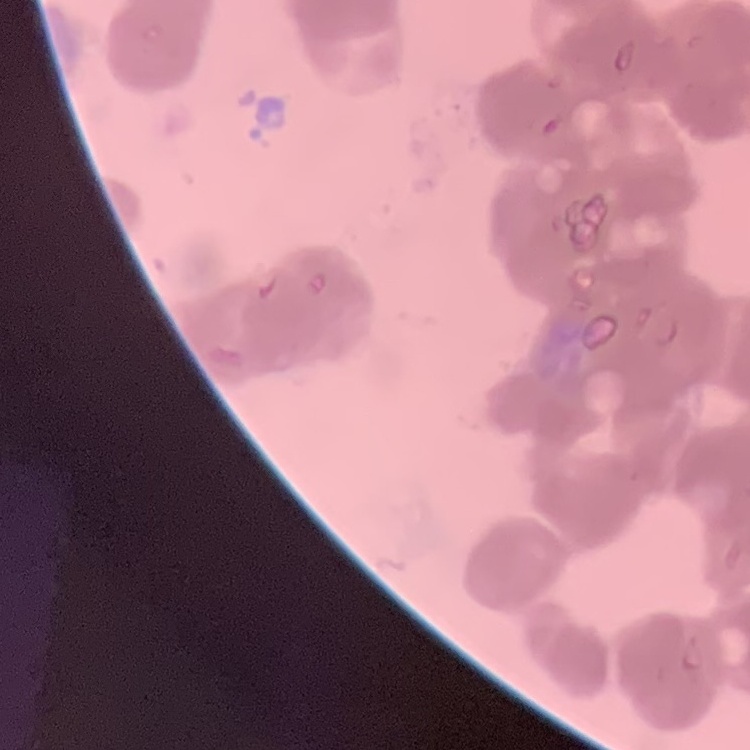
The erythrocytes exhibit rouleaux formation. Thin blood film. One tile cut from a larger photomicrograph. Stained with either Field's or Giemsa.